Give the position of every Plasmodium parasite.
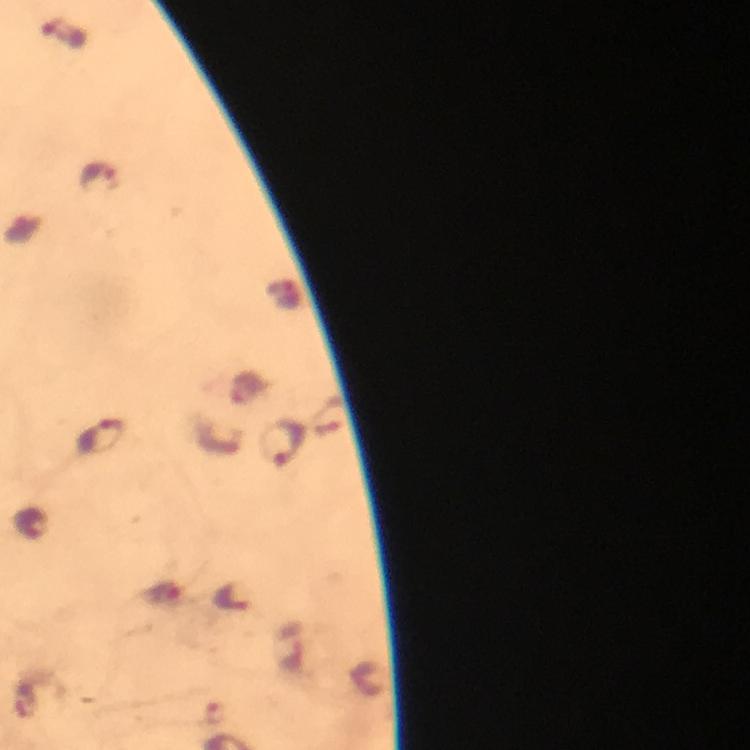
Approximate centers as [x, y] in pixels.
Plasmodium parasites: [64, 33], [98, 174], [102, 437], [284, 443], [30, 523], [164, 592], [231, 598].

preparation = thick blood film
context = from a malaria diagnostic workup
magnification = 100x
image size = 750×750 pixels
stain = Giemsa
capture = smartphone photograph through a microscope
immersion oil = used
cropped from = one field of view